Point out each malaria parasite and each leukocyte.
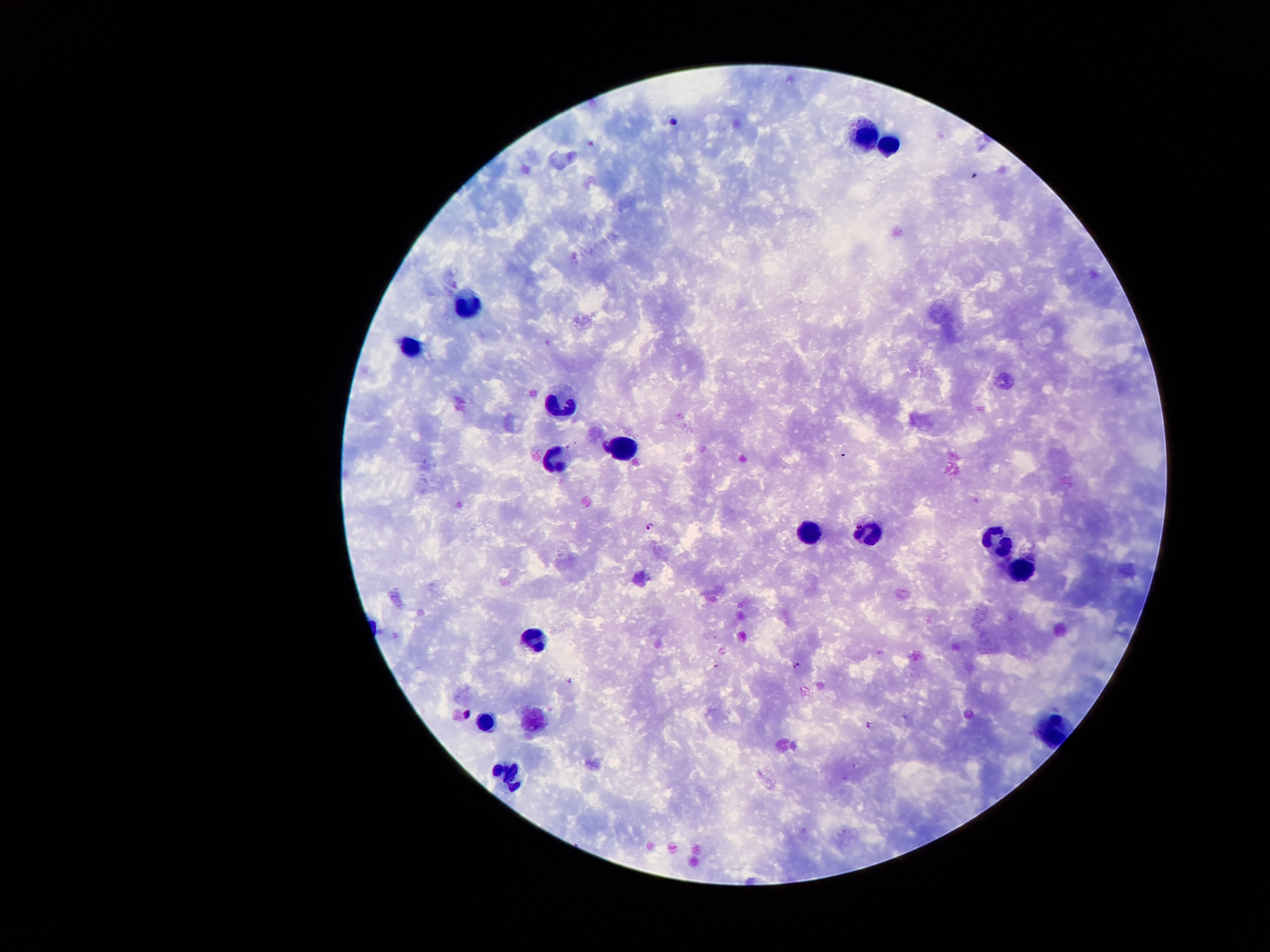
Approximate centers as (x, y) in pixels.
Malaria parasites: (673, 121), (570, 447), (651, 526), (797, 666), (570, 682), (467, 715), (870, 726).
Leukocytes: (866, 130), (889, 146), (473, 308), (416, 349), (559, 406), (624, 447), (551, 459), (808, 532), (870, 536), (992, 538), (1019, 566), (537, 637), (484, 724), (1046, 731), (504, 775).

Smartphone photograph taken through the microscope eyepiece. Image is 1270×952 pixels. 100x magnification. One field from this slide. Patient malaria status: positive for Plasmodium falciparum. Giemsa-stained preparation. Thick blood smear.